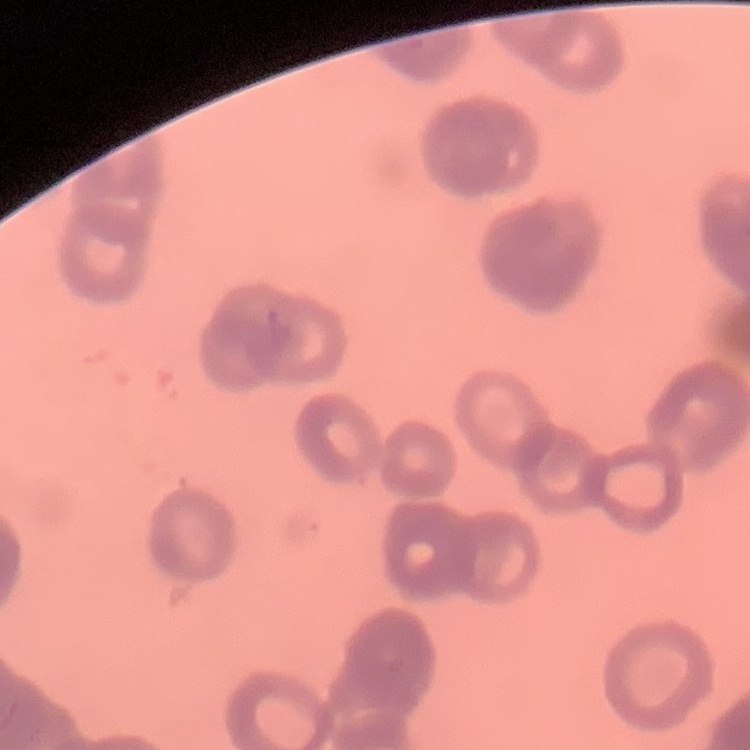 The erythrocytes show rouleaux formation. Square crop of a larger photomicrograph. Field's or Giemsa stain. Thin peripheral smear.